Locate every malaria parasite.
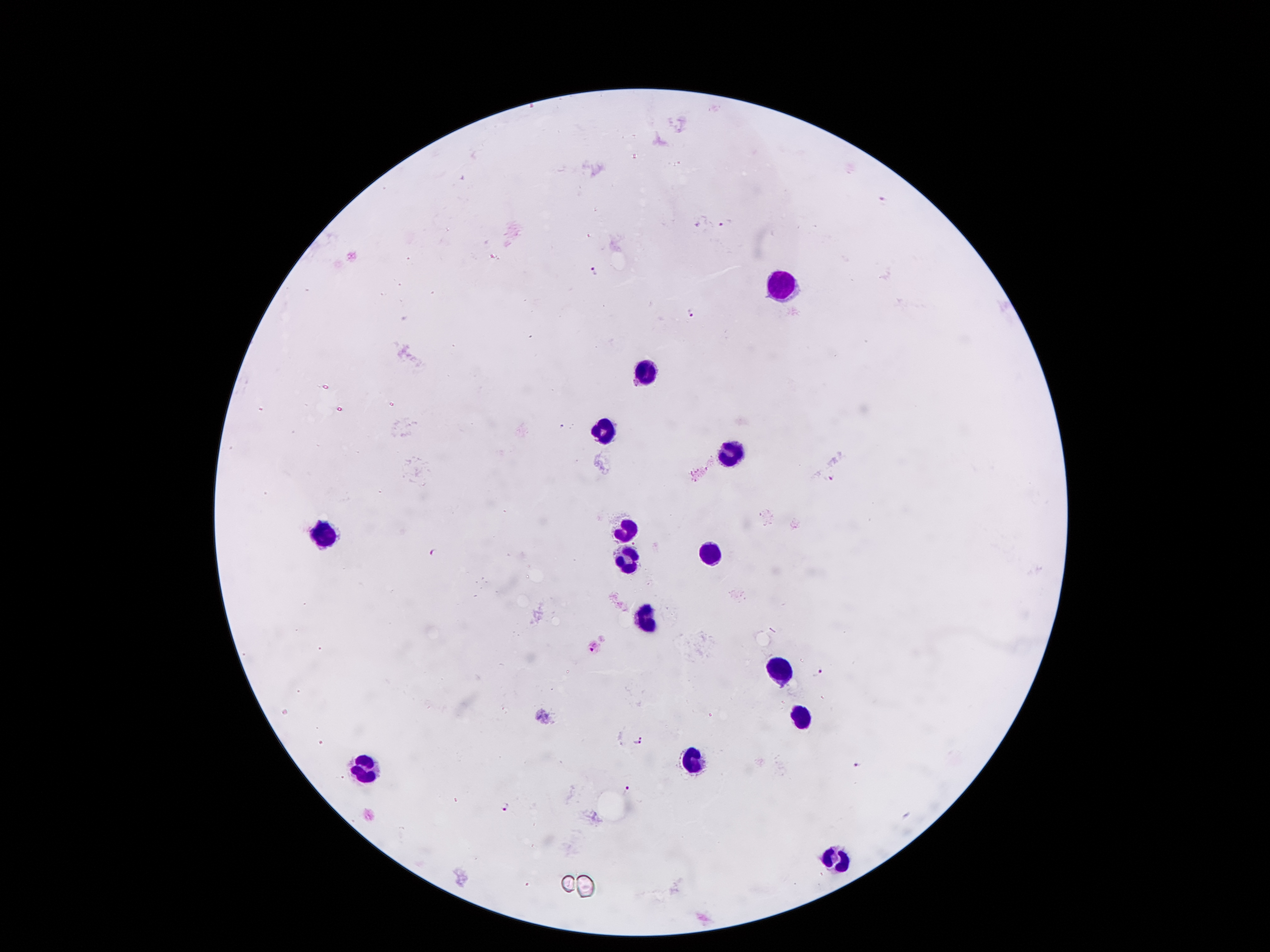

Approximate object centers, in pixels from the top-left corner.
Malaria parasites: (x=882, y=200), (x=722, y=224), (x=595, y=271), (x=694, y=313), (x=828, y=476), (x=432, y=552), (x=592, y=648), (x=818, y=672), (x=641, y=736), (x=638, y=743), (x=859, y=764), (x=628, y=789), (x=505, y=806).

Leukocyte locations: (x=775, y=287), (x=643, y=373), (x=607, y=434), (x=727, y=454), (x=625, y=527), (x=326, y=533), (x=707, y=554), (x=628, y=555), (x=646, y=620), (x=784, y=670), (x=793, y=713), (x=691, y=763), (x=362, y=766), (x=837, y=860). One field from this slide. Patient malaria status: positive for Plasmodium falciparum. Smartphone photograph taken through the microscope eyepiece. Thick blood film. 100x magnification. Image is 1270×952 pixels. Giemsa stain.